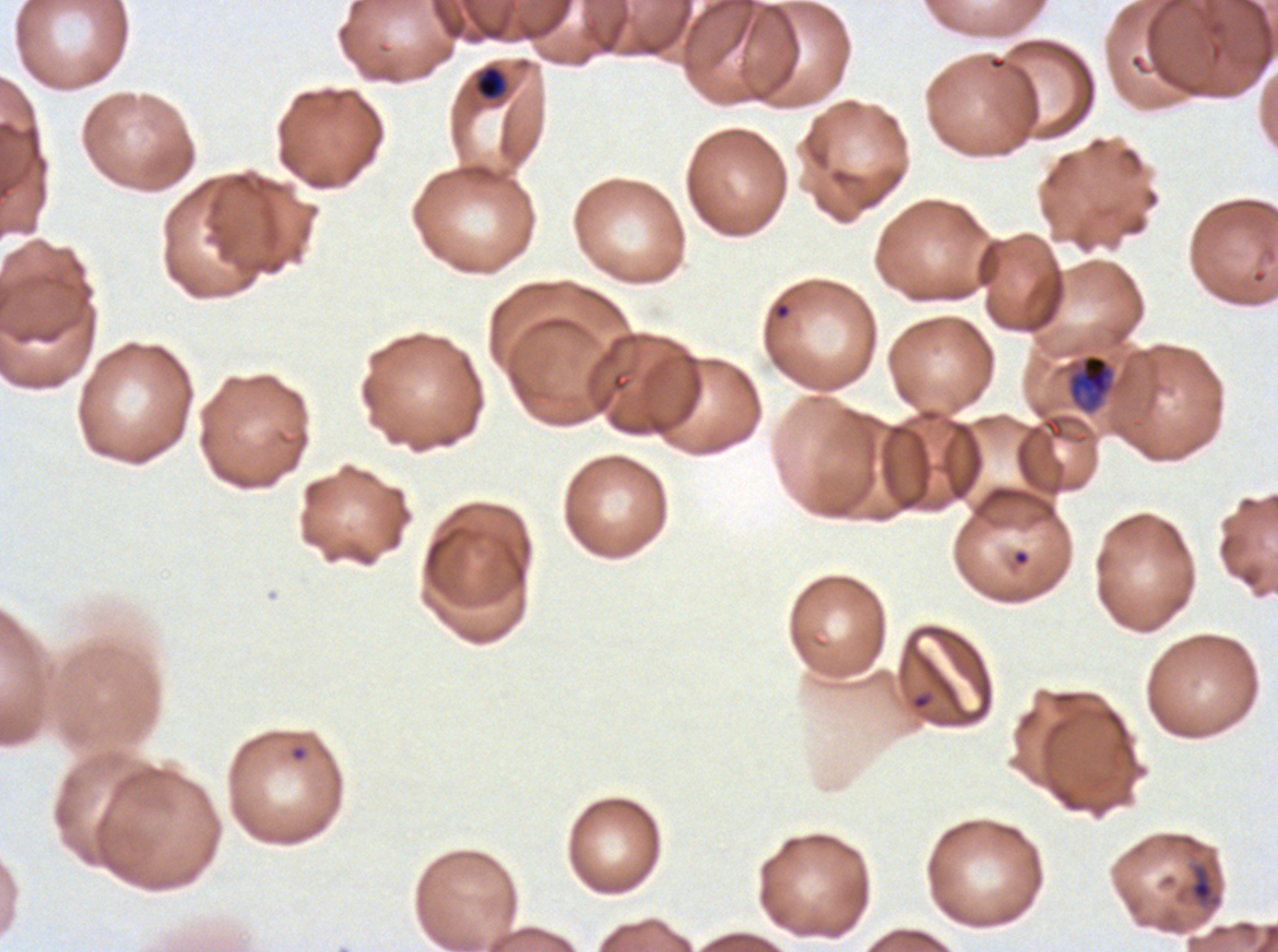
Approximate bounding boxes as (x1, y1, x2, y2) in pixels. Debris locations: (1188, 861, 1222, 908). Ring locations: (911, 692, 932, 711), (288, 743, 309, 763). Late-ring/early-trophozoite locations: (474, 65, 507, 101), (1067, 353, 1115, 413). Life-cycle stages observed: ring, late-ring/early-trophozoite. Thin blood smear. Plasmodium falciparum cultured ex vivo for 24 to 48 hours, from a patient in The Gambia. Giemsa stain. Image is 1278×952 pixels. A sub-image separated from a larger composite.